Report the malaria status of this cell.
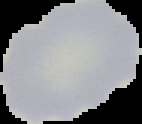

Uninfected.

The area outside the segmented cell region is set to black. Image is 142×124 pixels. From a thin blood film.